Point out each Plasmodium parasite.
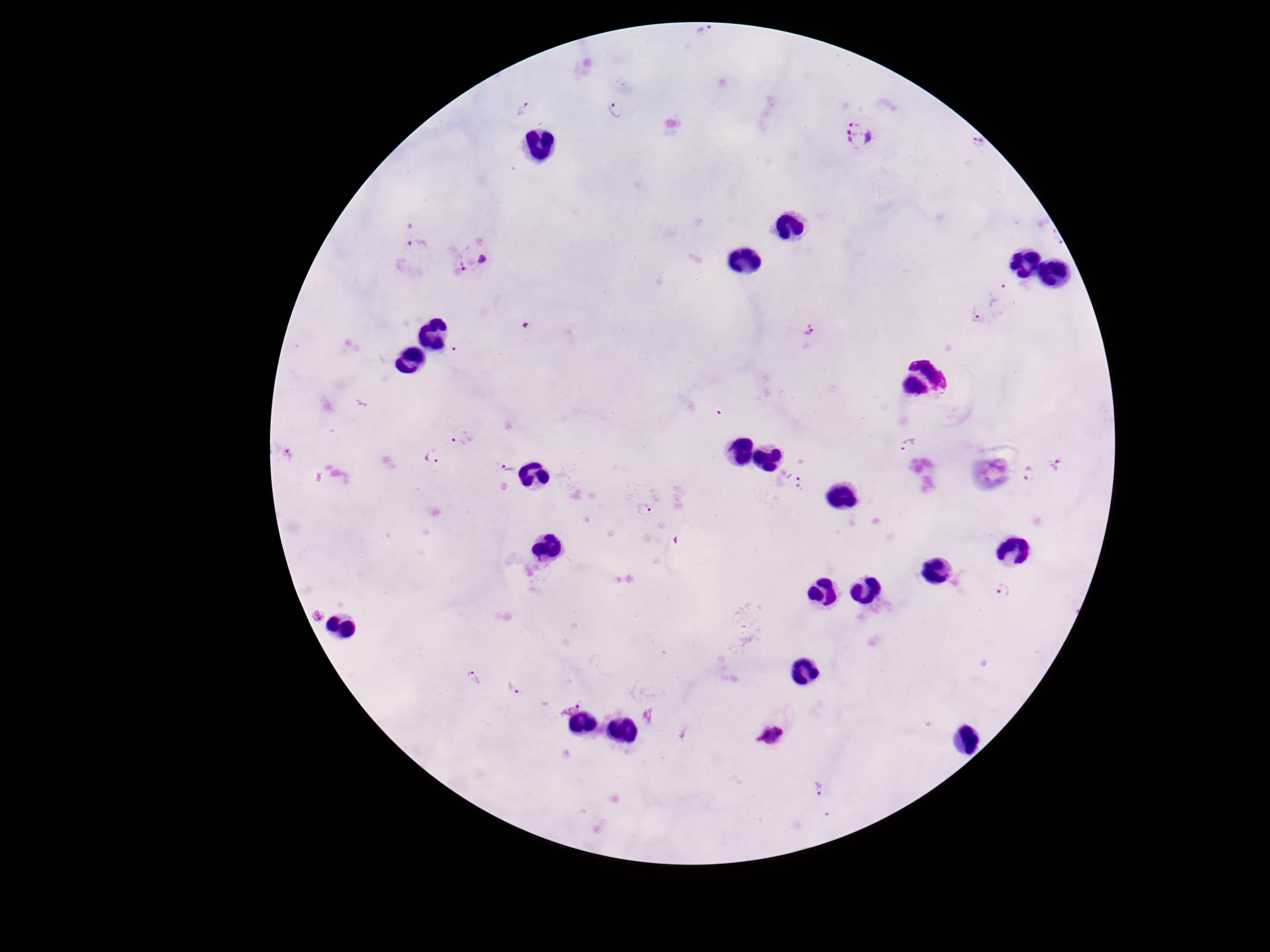

Approximate centers as {x, y} in pixels.
Plasmodium parasites: {523, 107}, {620, 110}, {858, 132}, {978, 145}, {1057, 239}, {418, 249}, {472, 257}, {999, 291}, {976, 320}, {811, 332}, {450, 354}, {461, 438}, {905, 445}, {432, 454}, {287, 456}, {1057, 463}, {505, 469}, {1030, 475}, {794, 479}, {644, 510}, {1002, 590}, {319, 615}, {473, 677}, {513, 688}, {569, 703}, {771, 734}, {817, 789}.

Summary:
  - Magnification: 100x
  - Stain: Giemsa
  - Capture: smartphone camera through the microscope eyepiece
  - Preparation: thick blood smear
  - Patient malaria status: infected
  - Image size: 1270×952 pixels
  - Field of view: one from this slide